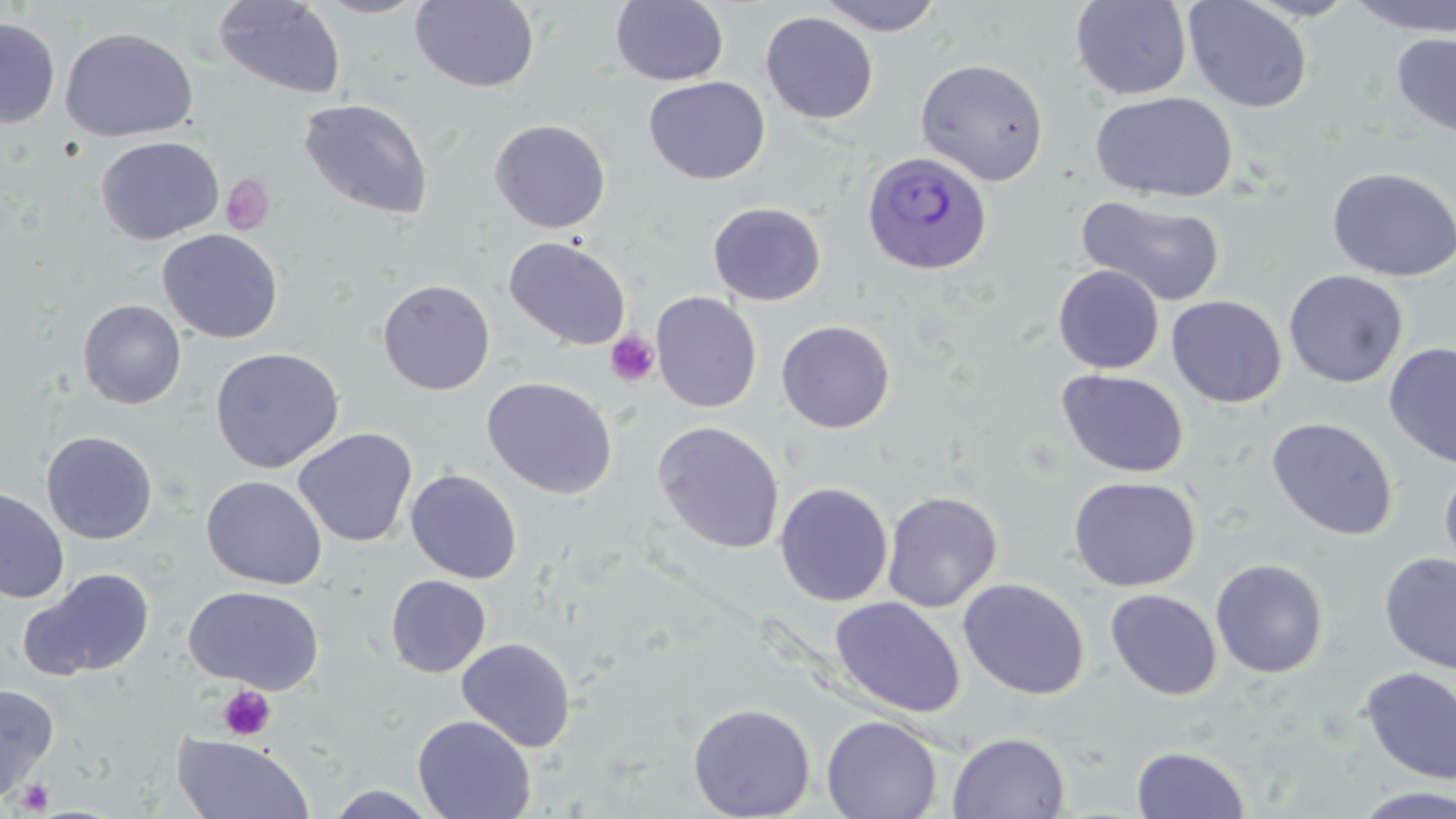

Approximate bounding boxes as [x1, y1, x2, y2] in pixels. Uninfected red blood cell locations: [213, 0, 347, 99], [313, 0, 429, 19], [816, 0, 944, 36], [1070, 0, 1192, 100], [1183, 0, 1313, 113], [1240, 0, 1360, 21], [1345, 0, 1456, 37], [410, 1, 540, 92], [610, 1, 729, 86], [760, 11, 878, 125], [0, 17, 60, 128], [60, 27, 197, 142], [1391, 32, 1456, 139], [914, 58, 1050, 186], [644, 76, 770, 185], [1090, 92, 1237, 203], [298, 98, 433, 219], [489, 119, 610, 233], [495, 122, 616, 351], [96, 136, 224, 245], [1326, 166, 1456, 281], [1078, 195, 1226, 307], [708, 202, 826, 306], [157, 229, 282, 343], [504, 235, 631, 350], [1053, 265, 1164, 374], [1283, 270, 1408, 388], [377, 279, 495, 395], [650, 292, 762, 413], [1166, 295, 1286, 407], [78, 299, 186, 409], [776, 320, 896, 433], [1382, 342, 1456, 470], [210, 347, 344, 473], [1056, 369, 1190, 478], [482, 376, 618, 499], [1267, 416, 1398, 541], [652, 421, 785, 554], [293, 427, 418, 548], [41, 431, 158, 544], [1439, 463, 1456, 578], [405, 469, 523, 584], [201, 475, 327, 590], [1068, 476, 1200, 592], [775, 481, 893, 606], [0, 486, 69, 604], [881, 490, 1003, 613], [1379, 551, 1456, 674], [1210, 558, 1329, 678], [22, 568, 155, 680], [385, 575, 491, 678], [958, 578, 1090, 700], [183, 586, 324, 693], [1105, 589, 1222, 701], [830, 597, 965, 718], [456, 637, 576, 753], [1359, 666, 1456, 784], [0, 682, 59, 801], [687, 702, 816, 819], [412, 714, 536, 819], [821, 715, 943, 819], [946, 732, 1071, 818], [172, 734, 315, 818], [1131, 745, 1250, 819], [322, 785, 444, 818], [1351, 786, 1456, 819]. Platelet locations: [220, 174, 275, 235], [606, 331, 660, 387], [217, 685, 276, 741], [15, 777, 55, 814]. Plasmodium ovale-infected red blood cell locations: [861, 150, 994, 275]. Slide-level diagnosis: Plasmodium ovale. Captured at 1000x magnification. Thin blood smear. Optical microscopy. May-Grünwald-Giemsa stain. Image is 1456×819 pixels. Single field of view.